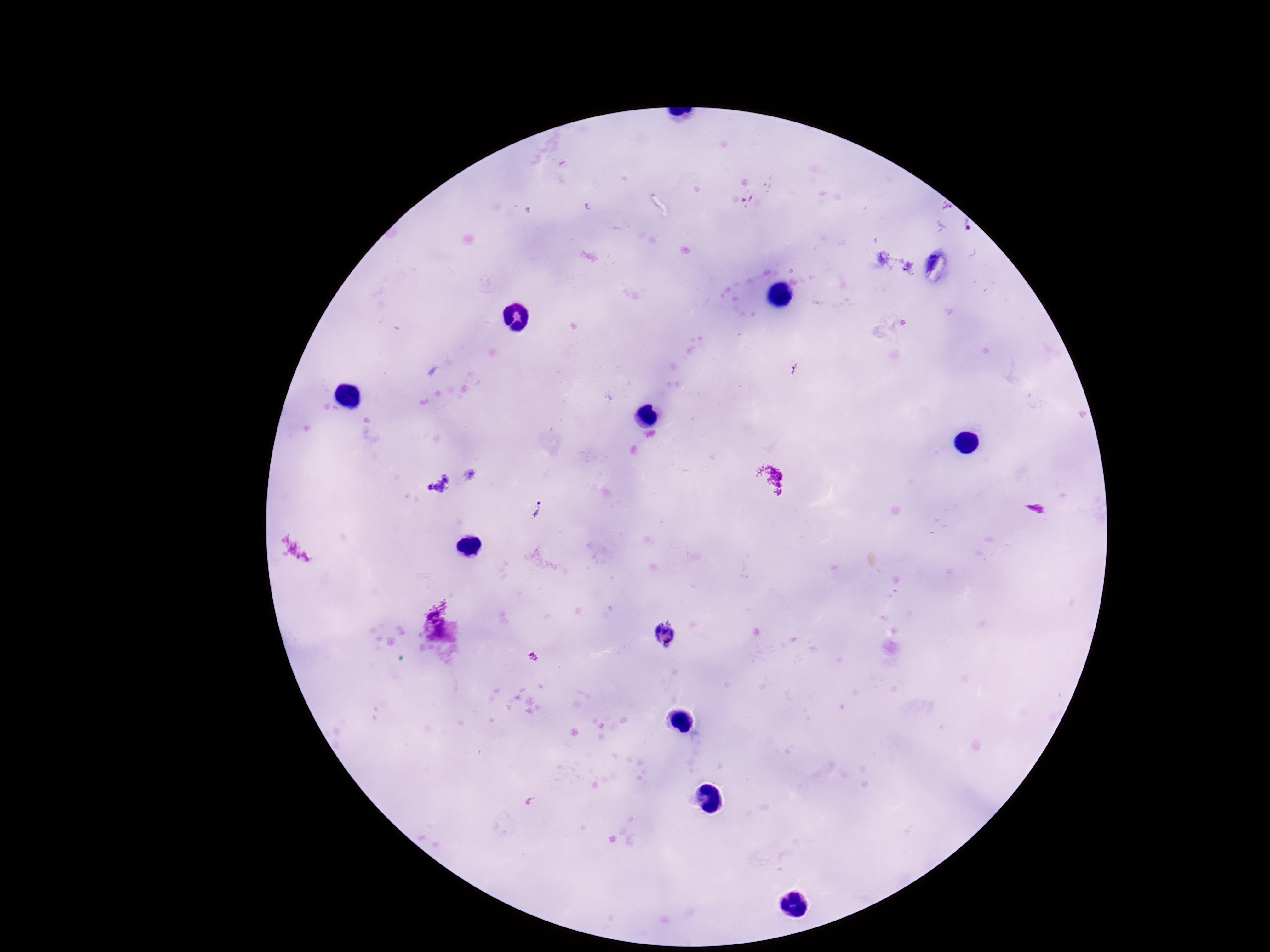

Approximate centers as [x, y] in pixels.
Summary:
  - Plasmodium parasite locations: [439, 484], [537, 511], [666, 633]
  - Patient malaria status: positive
  - Image size: 1270×952 pixels
  - Stain: Giemsa
  - Field of view: one from this slide
  - Capture: smartphone camera through the microscope eyepiece
  - Magnification: 100x
  - Preparation: thick blood film